Classify this cell by malaria status.
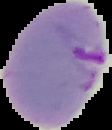
Parasitized.

image size = 112×130 pixels
image type = segmented cell region on a black background
preparation = thin blood film